State which parasite is depicted.
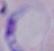
This is a trypanosome.

Summary:
  - Magnification: 1000x
  - Modality: micrograph